Point out every malaria parasite.
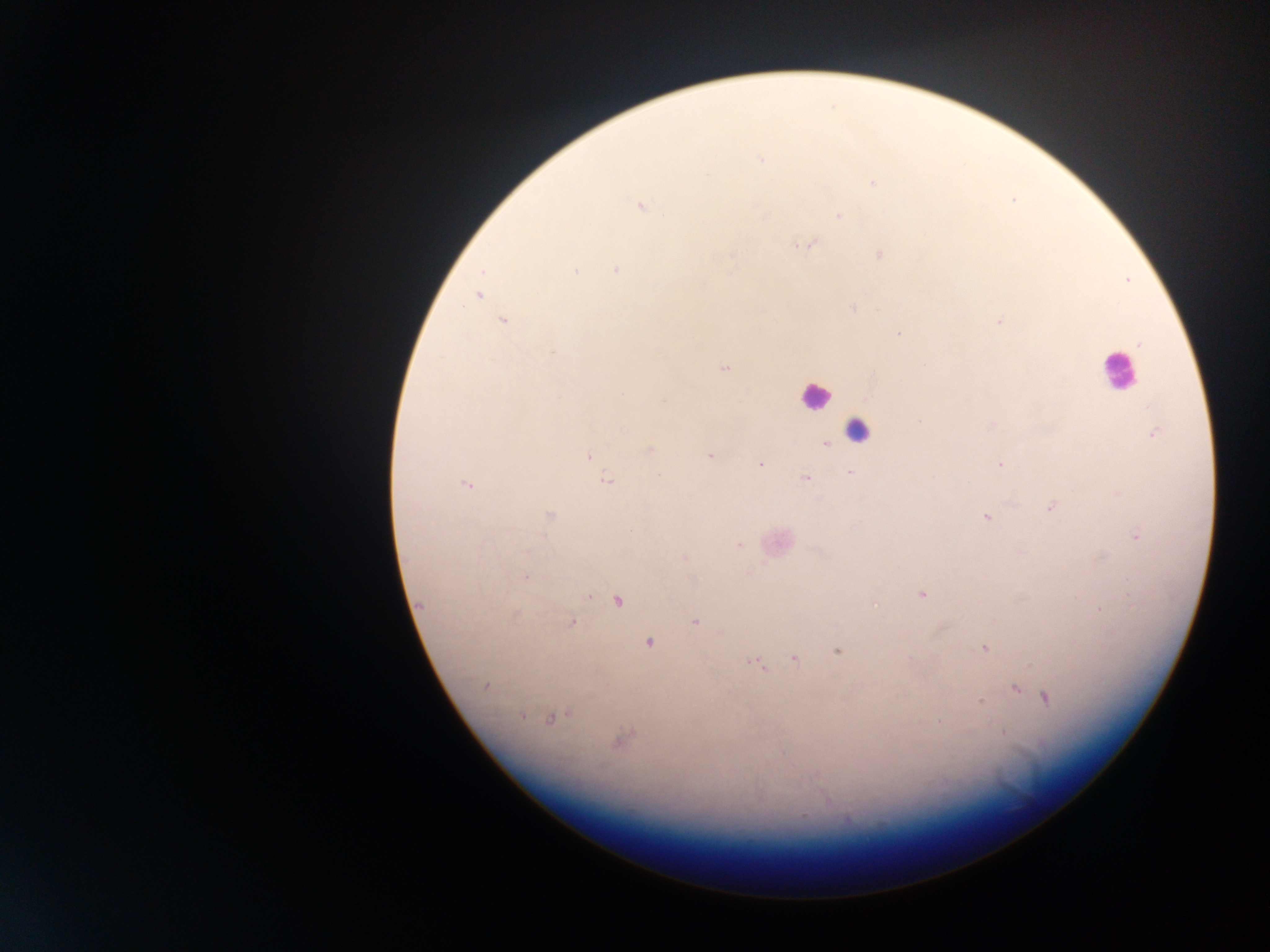
Approximate centers as (x, y) in pixels.
Malaria parasites: (760, 160), (873, 182), (640, 208), (839, 215), (808, 245), (880, 254), (732, 255), (616, 269), (483, 271), (574, 271), (703, 285), (478, 296), (853, 308), (503, 321), (999, 321), (899, 333), (1138, 344), (554, 351), (726, 368), (920, 420), (1156, 433), (826, 444), (650, 450), (709, 455), (588, 457), (759, 465), (1000, 465), (851, 473), (659, 475), (806, 478), (607, 482), (466, 483), (1050, 508), (549, 515), (986, 517), (1137, 537), (739, 545), (685, 557), (525, 578), (921, 595), (589, 596), (618, 601), (421, 604), (874, 604), (1100, 610), (516, 615), (695, 621), (571, 623), (649, 643), (984, 649), (838, 652), (793, 658), (757, 663), (485, 686), (1016, 690), (1045, 698), (981, 702), (521, 716), (550, 718), (939, 722), (1002, 731), (619, 741).

Leukocyte locations: (1116, 370), (815, 397), (859, 432), (778, 543). Image is 1270×952 pixels. Collected in Ghana. Thick blood film. Single field of view. Mobile-phone photograph taken through the microscope.